Identify the preparation type.
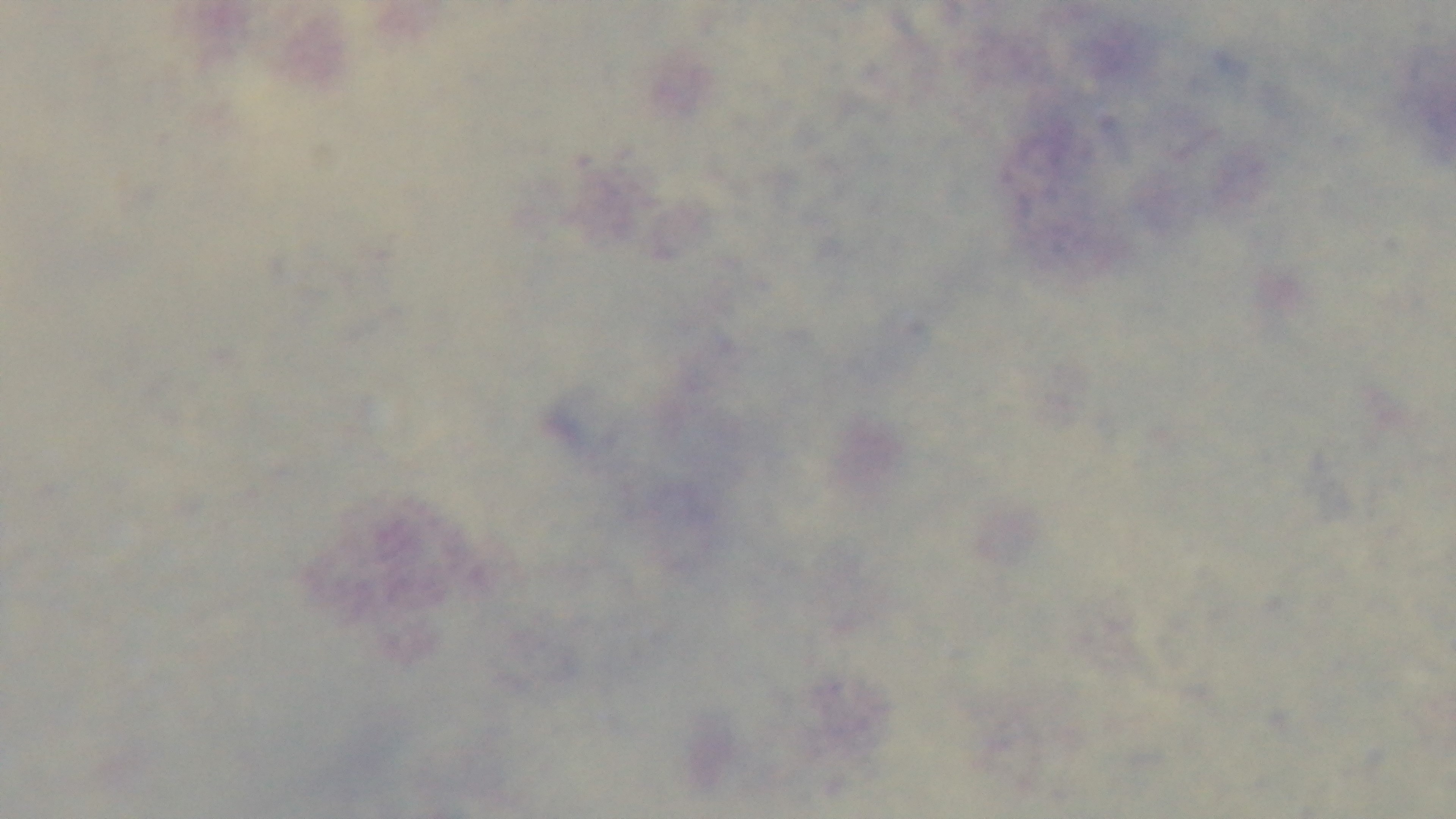

It is a thick blood film.

stain = Giemsa
capture = mounted 4K digital camera
field of view = single
modality = light microscopy
objective = 100x oil immersion
malaria status = uninfected